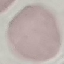

{
  "malaria_status": "uninfected",
  "capture": "smartphone through the microscope eyepiece",
  "stain": "Giemsa",
  "preparation": "thin blood film",
  "image_type": "automatically extracted cell patch, resized to 64 × 64 pixels"
}